Report the malaria status of this cell.
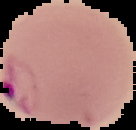

Parasitized.

From a thin blood smear. Image is 136×130 pixels. Segmented cell region on a black background.